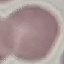

Summary:
  - Result: no malaria parasites detected
  - Image type: cell patch, automatically extracted from a larger field of view and resized to 64 × 64 pixels
  - Preparation: thin blood smear
  - Capture: smartphone camera at the microscope eyepiece
  - Stain: Giemsa